Assess this cell for malaria.
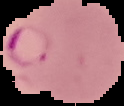

It is parasitized.

{
  "preparation": "thin blood film",
  "image_type": "cell region segmented out of the field of view; surrounding area masked to black",
  "image_size": "124×106 pixels"
}